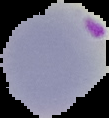

Summary:
  - Image size: 109×118 pixels
  - Image type: cell region segmented out of the field of view; surrounding area masked to black
  - Result: Plasmodium parasites identified
  - Preparation: thin blood smear